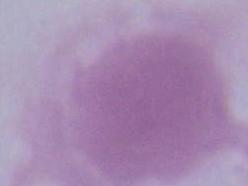
A red blood cell is shown. 1000x magnification. Micrograph.